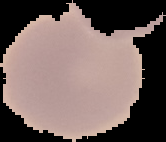
image_size: 166×142 pixels
preparation: thin blood smear
malaria_status: uninfected
image_type: cell region segmented out of the field of view; surrounding area masked to black